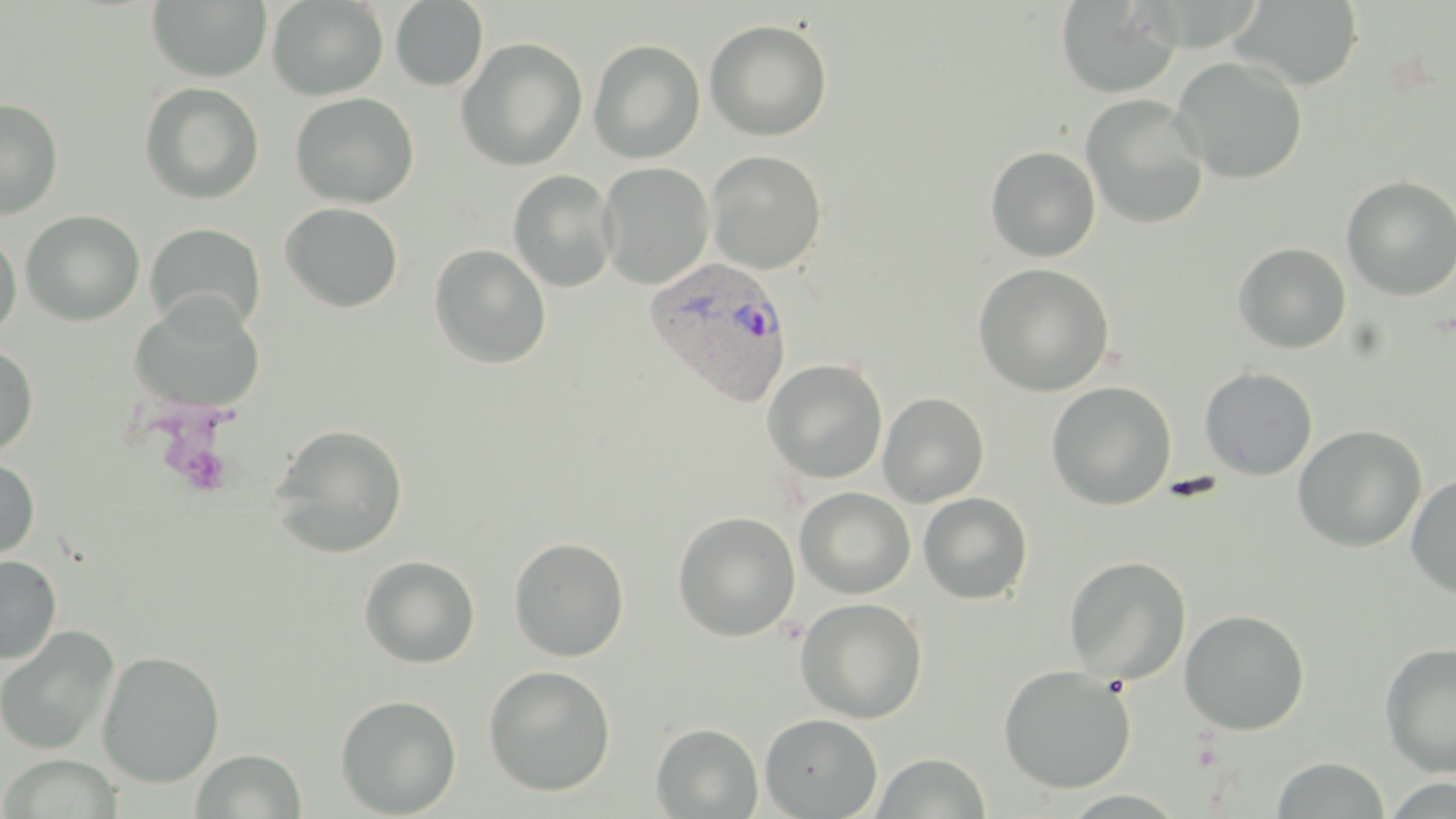

Approximate bounding boxes as (x1, y1, x2, y2) in pixels. Platelet locations: (179, 444, 234, 497), (1161, 474, 1225, 502). Plasmodium vivax-infected red blood cell locations: (644, 256, 794, 407). Uninfected red blood cell locations: (267, 0, 388, 100), (1231, 0, 1365, 92), (147, 1, 272, 83), (391, 1, 488, 90), (1056, 1, 1183, 99), (705, 20, 832, 140), (457, 38, 588, 171), (588, 40, 705, 163), (1172, 55, 1308, 184), (140, 82, 264, 204), (290, 92, 419, 208), (1081, 94, 1210, 229), (0, 98, 63, 219), (986, 146, 1101, 262), (706, 150, 827, 274), (597, 161, 715, 289), (508, 169, 618, 292), (1341, 175, 1456, 301), (280, 202, 404, 312), (21, 210, 145, 325), (144, 223, 266, 337), (0, 229, 22, 337), (1233, 242, 1352, 354), (429, 244, 551, 368), (973, 263, 1115, 397), (127, 295, 266, 414), (0, 344, 39, 457), (763, 359, 888, 484), (1199, 367, 1318, 480), (1046, 381, 1177, 509), (878, 391, 990, 507), (269, 423, 408, 558), (1292, 424, 1428, 552), (0, 456, 40, 561), (1405, 474, 1456, 598), (794, 487, 915, 599), (918, 492, 1033, 604), (673, 511, 800, 641), (509, 536, 629, 661), (360, 554, 481, 668), (0, 555, 62, 664), (1064, 555, 1191, 684), (795, 597, 928, 723), (1179, 609, 1311, 735), (0, 625, 120, 756), (1379, 642, 1456, 777), (97, 649, 224, 787), (998, 664, 1136, 793), (483, 665, 616, 797), (335, 694, 461, 818), (759, 713, 883, 818), (651, 723, 763, 818), (192, 749, 307, 819), (871, 752, 991, 818), (1, 754, 123, 818), (1272, 757, 1392, 817). Slide-level diagnosis: Plasmodium vivax. Image is 1456×819 pixels. May-Grünwald-Giemsa-stained preparation. Thin blood smear. Single field of view. Light microscopy. Captured at 1000x magnification.